Assess this cell for malaria.
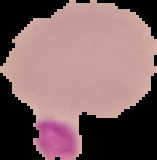

Uninfected.

Image is 157×160 pixels. Segmented cell region on a black background. From a thin blood film.